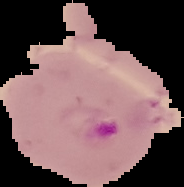
Summary:
  - Result: Plasmodium parasites detected
  - Preparation: thin blood film
  - Image type: segmented cell region with the area outside set to black
  - Image size: 184×187 pixels